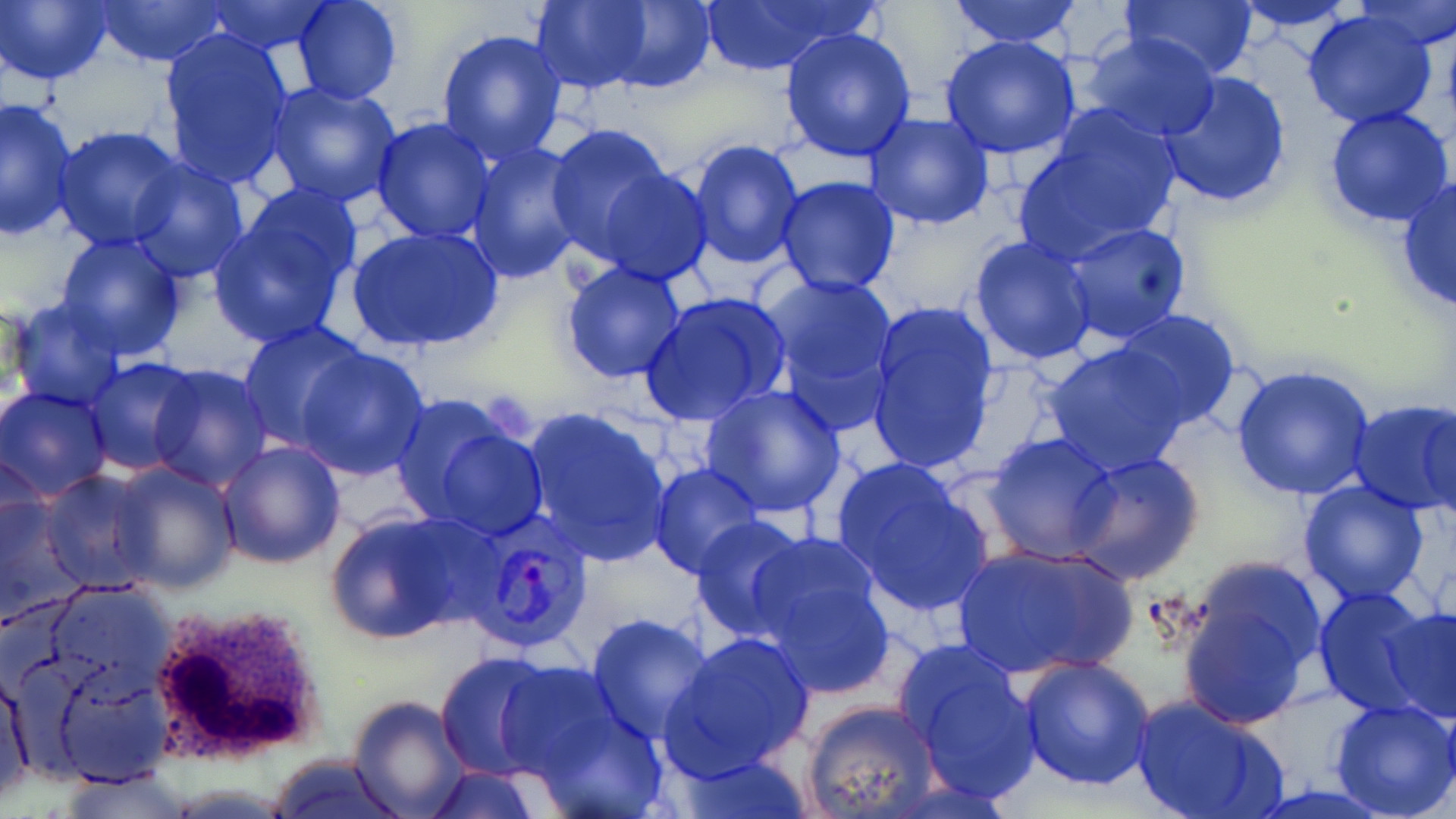

Approximate bounding boxes as named x1/y1/x2/y2 corners in pixels. Uninfected red blood cell locations: (x1=0, y1=0, x2=115, y2=86), (x1=291, y1=0, x2=404, y2=105), (x1=529, y1=0, x2=654, y2=92), (x1=601, y1=0, x2=715, y2=94), (x1=693, y1=0, x2=876, y2=75), (x1=948, y1=0, x2=1085, y2=50), (x1=1124, y1=0, x2=1259, y2=83), (x1=1350, y1=0, x2=1456, y2=50), (x1=91, y1=1, x2=229, y2=67), (x1=202, y1=1, x2=335, y2=55), (x1=1226, y1=1, x2=1361, y2=33), (x1=1299, y1=7, x2=1441, y2=128), (x1=779, y1=26, x2=918, y2=162), (x1=158, y1=27, x2=293, y2=187), (x1=437, y1=28, x2=566, y2=164), (x1=1080, y1=32, x2=1221, y2=142), (x1=939, y1=33, x2=1081, y2=158), (x1=1157, y1=70, x2=1292, y2=209), (x1=265, y1=82, x2=403, y2=210), (x1=1, y1=96, x2=79, y2=240), (x1=1017, y1=106, x2=1182, y2=258), (x1=1322, y1=106, x2=1454, y2=230), (x1=864, y1=111, x2=995, y2=230), (x1=370, y1=117, x2=495, y2=244), (x1=545, y1=123, x2=679, y2=262), (x1=53, y1=124, x2=187, y2=250), (x1=686, y1=137, x2=807, y2=270), (x1=464, y1=142, x2=589, y2=283), (x1=125, y1=154, x2=251, y2=282), (x1=591, y1=163, x2=716, y2=284), (x1=1395, y1=174, x2=1456, y2=316), (x1=775, y1=176, x2=903, y2=296), (x1=208, y1=190, x2=364, y2=352), (x1=1055, y1=222, x2=1191, y2=346), (x1=348, y1=226, x2=505, y2=353), (x1=55, y1=233, x2=189, y2=360), (x1=969, y1=235, x2=1098, y2=366), (x1=559, y1=262, x2=687, y2=384), (x1=760, y1=273, x2=900, y2=405), (x1=639, y1=291, x2=791, y2=425), (x1=6, y1=297, x2=126, y2=411), (x1=864, y1=299, x2=999, y2=473), (x1=1113, y1=310, x2=1244, y2=432), (x1=238, y1=322, x2=371, y2=451), (x1=1043, y1=341, x2=1190, y2=475), (x1=293, y1=345, x2=433, y2=480), (x1=81, y1=357, x2=203, y2=475), (x1=146, y1=362, x2=271, y2=489), (x1=1229, y1=364, x2=1377, y2=501), (x1=0, y1=384, x2=113, y2=502), (x1=699, y1=384, x2=849, y2=520), (x1=390, y1=396, x2=546, y2=537), (x1=1346, y1=399, x2=1456, y2=517), (x1=1419, y1=400, x2=1456, y2=523), (x1=519, y1=406, x2=673, y2=567), (x1=983, y1=432, x2=1119, y2=564), (x1=217, y1=440, x2=347, y2=569), (x1=2, y1=448, x2=51, y2=563), (x1=1067, y1=452, x2=1205, y2=585), (x1=830, y1=454, x2=993, y2=615), (x1=107, y1=460, x2=239, y2=594), (x1=649, y1=463, x2=766, y2=578), (x1=40, y1=470, x2=157, y2=593), (x1=1297, y1=481, x2=1431, y2=605), (x1=1, y1=490, x2=85, y2=624), (x1=322, y1=510, x2=486, y2=645), (x1=689, y1=517, x2=814, y2=641), (x1=745, y1=534, x2=897, y2=698), (x1=950, y1=542, x2=1138, y2=680), (x1=1176, y1=554, x2=1329, y2=724), (x1=38, y1=580, x2=178, y2=699), (x1=1313, y1=587, x2=1441, y2=717), (x1=1380, y1=601, x2=1456, y2=723), (x1=586, y1=612, x2=711, y2=742), (x1=661, y1=631, x2=817, y2=779), (x1=892, y1=636, x2=1042, y2=805), (x1=433, y1=652, x2=560, y2=780), (x1=1015, y1=655, x2=1156, y2=792), (x1=499, y1=658, x2=630, y2=786), (x1=1, y1=664, x2=35, y2=804), (x1=47, y1=669, x2=171, y2=788), (x1=346, y1=694, x2=470, y2=818), (x1=526, y1=694, x2=665, y2=819), (x1=1130, y1=694, x2=1288, y2=819), (x1=1329, y1=699, x2=1456, y2=819), (x1=801, y1=700, x2=939, y2=819), (x1=672, y1=751, x2=815, y2=818), (x1=262, y1=756, x2=413, y2=817), (x1=420, y1=766, x2=543, y2=818). White blood cell locations: (x1=144, y1=604, x2=322, y2=762). Plasmodium vivax-infected red blood cell locations: (x1=461, y1=516, x2=594, y2=651). Platelet locations: (x1=490, y1=390, x2=533, y2=437). Slide-level diagnosis: Plasmodium vivax. May-Grünwald-Giemsa-stained preparation. Single field of view. Optical microscopy. 1000x magnification. Thin blood smear. Image is 1456×819 pixels.